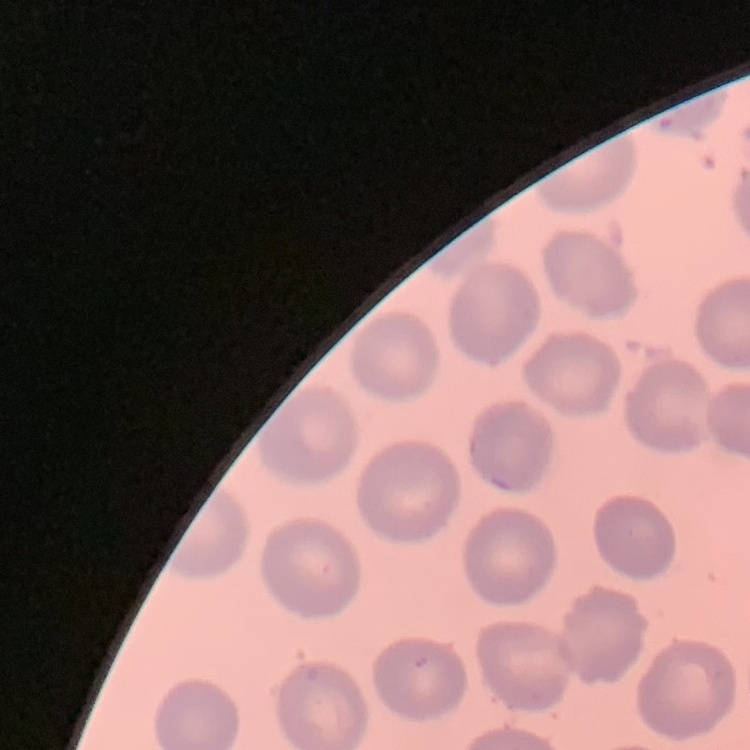
erythrocyte_morphology: no rouleaux formation
image_type: one tile cut from a larger photomicrograph
stain: Field's or Giemsa
preparation: thin blood film